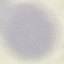

result = no malaria parasites seen
stain = Giemsa
image type = cell patch, automatically extracted from a larger field of view and resized to 64 × 64 pixels
preparation = thin smear
capture = smartphone camera at the microscope eyepiece